Locate every Plasmodium falciparum-infected red blood cell.
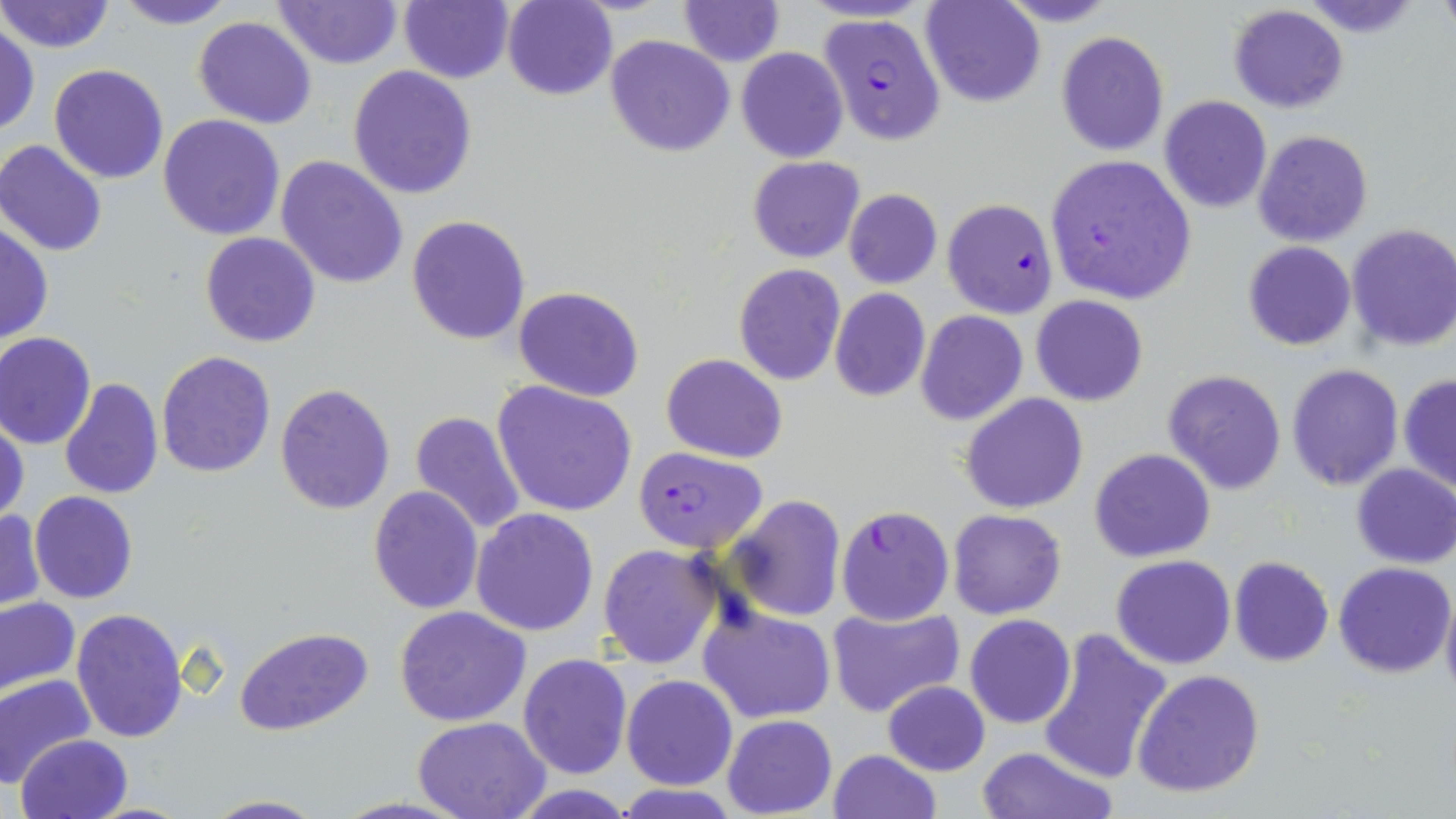

Approximate bounding boxes as (x1, y1, x2, y2) in pixels.
Plasmodium falciparum-infected red blood cells: (820, 14, 945, 143), (1043, 154, 1197, 307), (943, 197, 1058, 318), (636, 447, 773, 551), (836, 505, 952, 623).

Uninfected red blood cell locations: (113, 0, 239, 27), (398, 0, 513, 84), (501, 0, 617, 100), (678, 0, 784, 65), (921, 0, 1042, 107), (1, 1, 115, 54), (272, 1, 403, 70), (1227, 4, 1348, 113), (193, 17, 316, 129), (1, 23, 39, 136), (1055, 30, 1170, 156), (605, 35, 735, 157), (736, 47, 849, 162), (48, 64, 169, 183), (348, 65, 478, 199), (1159, 96, 1272, 212), (158, 114, 287, 240), (1252, 129, 1374, 247), (0, 139, 111, 256), (275, 155, 408, 289), (747, 156, 864, 263), (844, 189, 943, 290), (407, 214, 530, 344), (0, 223, 53, 343), (1345, 224, 1456, 353), (200, 232, 321, 348), (1242, 241, 1357, 350), (732, 263, 846, 385), (514, 286, 645, 401), (829, 288, 930, 402), (1030, 295, 1149, 406), (915, 311, 1027, 426), (0, 332, 96, 449), (155, 350, 275, 477), (661, 354, 787, 461), (1287, 364, 1403, 490), (1162, 370, 1287, 494), (1397, 373, 1456, 494), (60, 377, 164, 501), (492, 380, 638, 518), (275, 383, 396, 515), (961, 393, 1089, 514), (410, 409, 527, 536), (1, 415, 27, 524), (1089, 447, 1216, 563), (1351, 465, 1456, 568), (368, 486, 484, 614), (29, 491, 138, 603), (726, 495, 845, 621), (947, 508, 1067, 618), (472, 509, 599, 635), (1, 510, 44, 611), (597, 543, 723, 669), (1111, 554, 1236, 670), (1229, 555, 1333, 667), (1334, 561, 1453, 678), (1440, 583, 1456, 706), (0, 597, 81, 695), (392, 606, 533, 728), (699, 606, 837, 724), (71, 607, 190, 742), (827, 607, 965, 719), (965, 614, 1076, 729), (234, 627, 373, 735), (1037, 627, 1173, 784), (518, 652, 632, 777), (1132, 668, 1264, 797), (0, 673, 96, 788), (622, 676, 737, 790), (883, 680, 990, 776), (721, 715, 836, 818), (413, 717, 553, 818), (16, 734, 131, 819), (974, 746, 1120, 819), (827, 749, 941, 819), (612, 784, 745, 818), (201, 794, 326, 818). Slide-level diagnosis: Plasmodium falciparum. May-Grünwald-Giemsa stain. Image is 1456×819 pixels. Single field of view. Thin blood smear. Light microscopy. Captured at 1000x magnification.